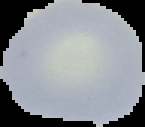
From a thin blood smear. Cell region segmented out of the field of view; the surrounding area is masked to black. Result: negative for Plasmodium parasites. Image is 145×127 pixels.